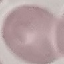

Summary:
  - Malaria status: uninfected
  - Stain: Giemsa
  - Preparation: thin smear
  - Image type: cell patch, automatically extracted from a larger field of view and resized to 64 × 64 pixels
  - Capture: smartphone camera at the microscope eyepiece